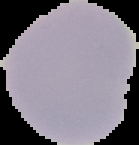 The area outside the segmented cell region is set to black. Image is 139×145 pixels. Malaria status: uninfected. From a thin blood film.